Describe the morphology of the red blood cells.
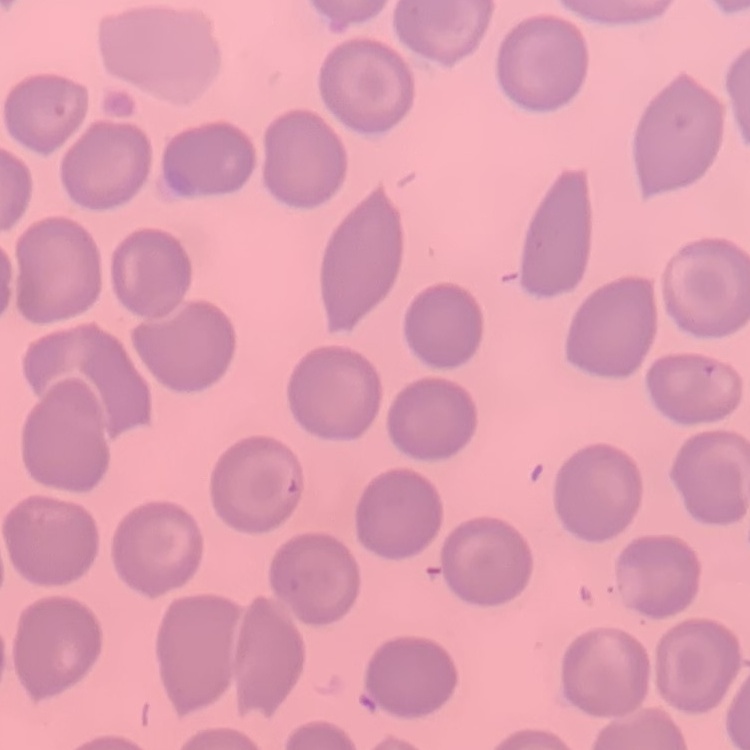

They show no rouleaux formation.

Thin peripheral smear. Stained with either Field's or Giemsa. Square crop of a larger photomicrograph.